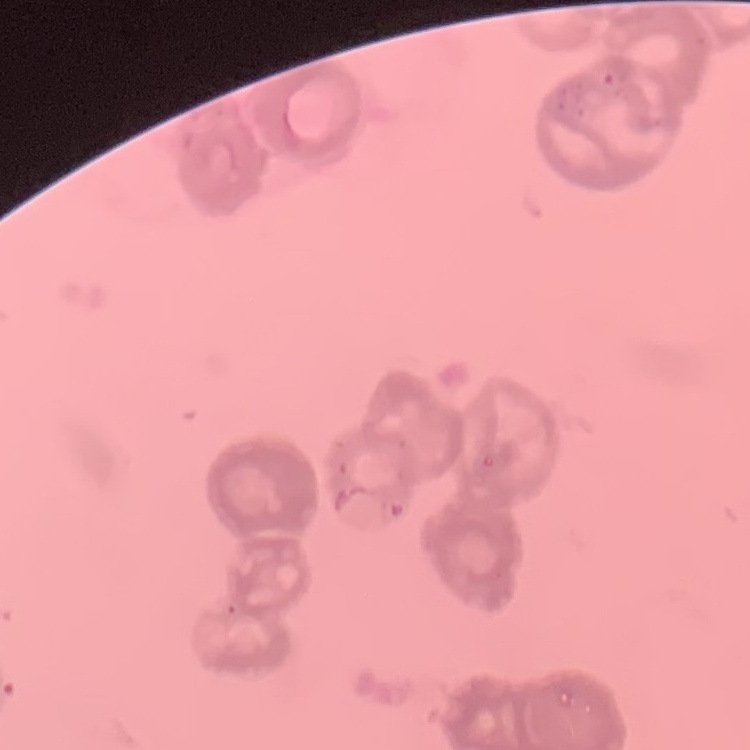

The red blood cells exhibit rouleaux formation. Thin peripheral smear. Field's or Giemsa stain. One tile cut from a larger photomicrograph.